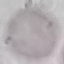 Result: no malaria parasites detected. Cell patch, automatically extracted from a larger field of view and resized to 64 × 64 pixels. Giemsa-stained preparation. Thin blood film. Acquired by smartphone through the microscope eyepiece.